Outline each blood parasite and name the species.
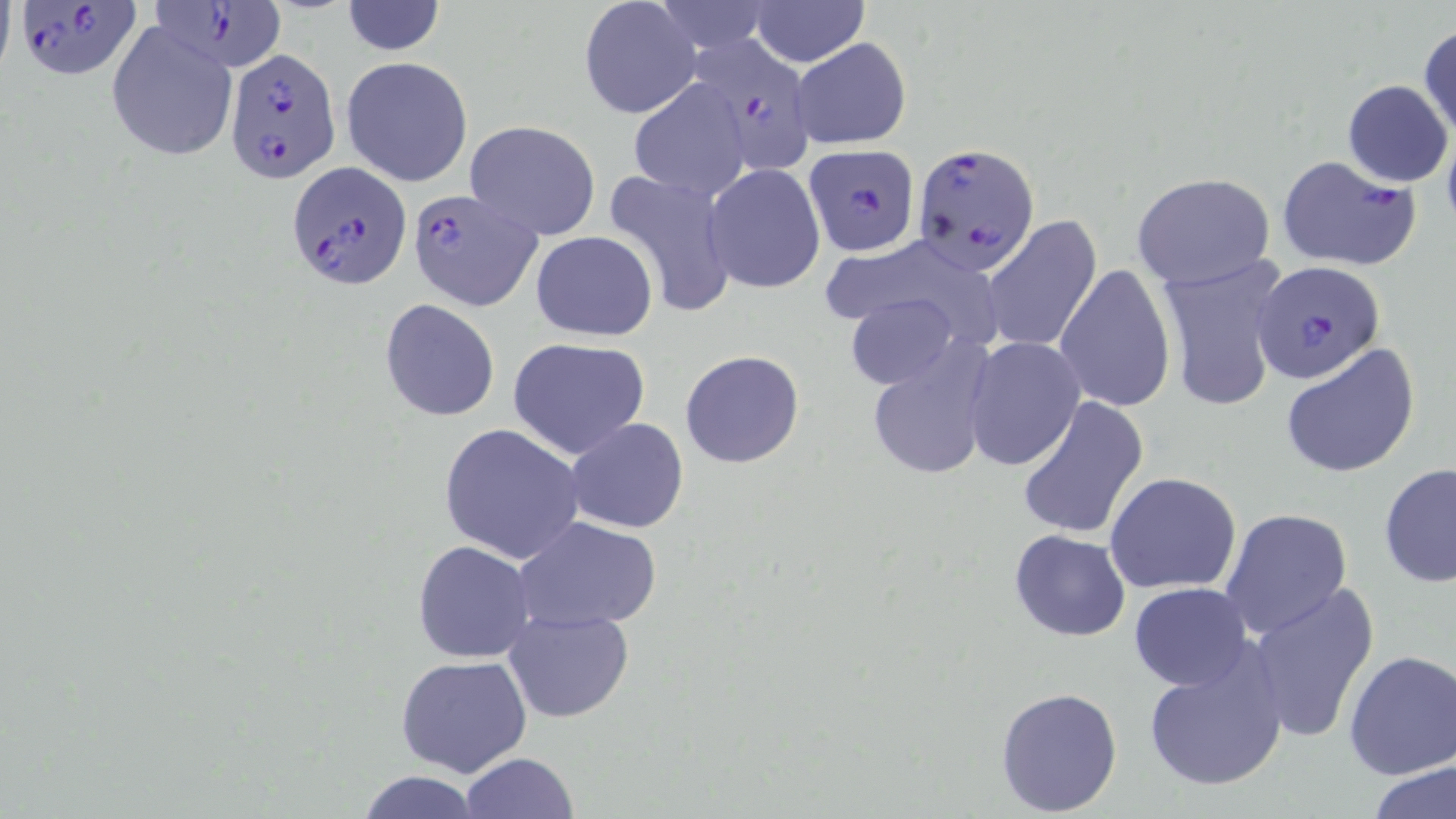
Approximate bounding boxes as (x1,y1)-(x2,y2) corner pairs in pixels.
Plasmodium falciparum-infected red blood cells: (13,0)-(142,81), (148,1)-(287,72), (681,35)-(815,176), (224,50)-(341,181), (913,141)-(1039,272), (804,145)-(920,257), (1275,154)-(1421,272), (288,160)-(411,291), (409,189)-(543,310), (1254,260)-(1388,385).
No Plasmodium ovale, Plasmodium malariae, Plasmodium vivax, Babesia divergens, or Trypanosoma brucei observed.

Summary:
  - Uninfected red blood cell locations: (579,0)-(701,120), (649,0)-(776,54), (341,1)-(446,56), (750,1)-(867,66), (105,20)-(237,162), (1417,25)-(1455,142), (790,36)-(912,150), (341,56)-(474,188), (625,79)-(753,202), (1342,79)-(1451,186), (463,120)-(602,240), (703,163)-(826,293), (602,168)-(738,317), (1132,173)-(1275,288), (983,217)-(1102,354), (530,231)-(657,340), (1158,252)-(1290,412), (1055,264)-(1176,413), (844,291)-(960,391), (380,298)-(500,422), (507,336)-(653,461), (963,336)-(1085,469), (866,342)-(996,482), (1280,343)-(1422,478), (679,350)-(805,468), (1017,397)-(1149,540), (564,417)-(689,534), (438,422)-(586,565), (1379,463)-(1456,590), (1104,472)-(1242,593), (1219,508)-(1352,639), (516,516)-(663,634), (1010,530)-(1130,641), (411,540)-(537,663), (1245,582)-(1379,744), (1129,583)-(1253,690), (501,609)-(635,722), (1141,643)-(1289,794), (1342,648)-(1456,779), (394,653)-(533,777), (995,685)-(1124,816), (461,751)-(578,818), (1369,760)-(1456,818), (353,770)-(485,818)
  - Slide-level diagnosis: Plasmodium falciparum
  - Field of view: single
  - Preparation: thin blood film
  - Magnification: 1000x
  - Modality: light microscopy
  - Stain: May-Grünwald-Giemsa
  - Image size: 1456×819 pixels